Assess this cell for malaria.
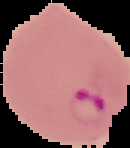

It is parasitized.

image type = segmented cell region on a black background
preparation = thin blood film
image size = 130×148 pixels